Report the malaria status of this cell.
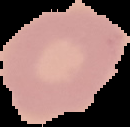
Uninfected.

Image is 130×127 pixels. Segmented cell region on a black background. From a thin blood film.